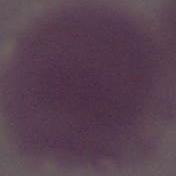

modality = photomicrograph
magnification = 1000x
identification = red blood cell